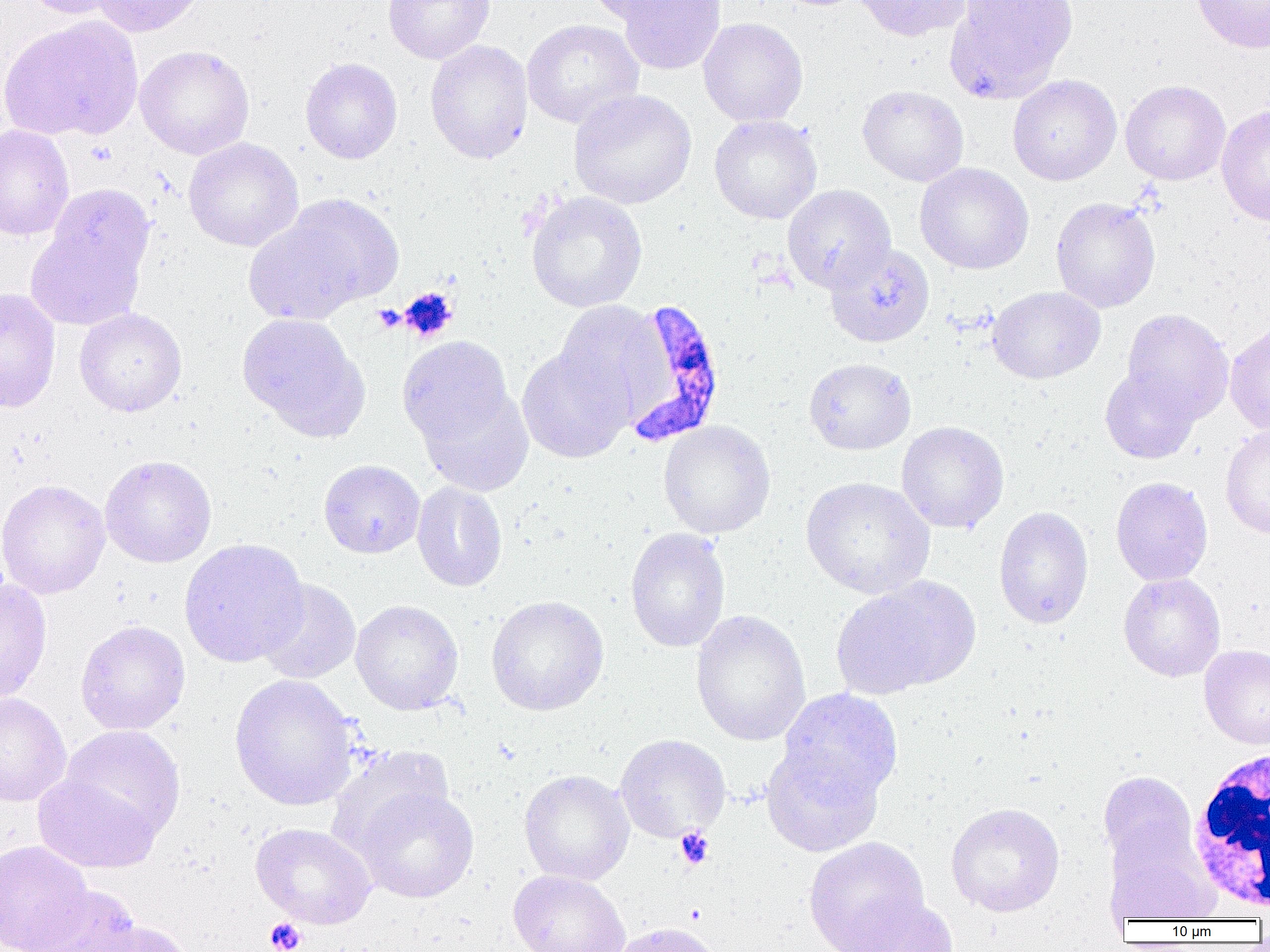
Approximate bounding boxes as (x1,y1)-(x2,y2) corner pairs in pixels. White blood cell locations: (1187,748)-(1270,913). Platelet locations: (397,288)-(458,341), (674,827)-(714,870), (264,917)-(307,952). Plasmodium falciparum-infected red blood cell locations: (619,298)-(727,446). Uninfected red blood cell locations: (21,0)-(131,19), (90,0)-(210,37), (383,0)-(495,64), (585,0)-(697,24), (615,0)-(726,75), (853,0)-(973,42), (945,0)-(1078,100), (1192,0)-(1270,53), (0,17)-(142,141), (698,17)-(808,127), (522,19)-(643,128), (425,39)-(534,164), (134,44)-(255,160), (300,57)-(403,164), (1007,74)-(1122,185), (1120,79)-(1231,186), (857,85)-(969,186), (568,89)-(696,210), (1216,104)-(1270,226), (709,114)-(822,224), (0,125)-(75,241), (183,137)-(304,251), (915,163)-(1034,274), (47,184)-(154,285), (782,184)-(895,293), (525,191)-(647,313), (280,193)-(404,306), (1050,197)-(1161,313), (243,214)-(367,326), (26,223)-(146,331), (824,242)-(935,348), (987,286)-(1105,384), (0,287)-(61,413), (553,300)-(668,424), (74,308)-(187,417), (1122,308)-(1234,423), (237,313)-(367,438), (1225,323)-(1270,435), (397,336)-(514,449), (517,347)-(633,463), (804,358)-(916,455), (1100,365)-(1201,464), (417,385)-(534,496), (658,420)-(776,539), (896,421)-(1009,534), (1220,423)-(1270,539), (99,455)-(217,568), (318,459)-(425,558), (1111,476)-(1213,586), (800,477)-(934,598), (0,479)-(110,600), (411,481)-(507,592), (993,506)-(1094,629), (625,527)-(731,653), (178,538)-(309,668), (1118,573)-(1226,682), (832,577)-(978,697), (0,579)-(52,705), (256,579)-(361,684), (486,595)-(609,716), (350,599)-(464,715), (690,609)-(811,747), (75,620)-(190,735), (1199,645)-(1270,750), (229,674)-(360,811), (777,688)-(904,805), (0,692)-(71,807), (60,725)-(185,840), (615,734)-(731,842), (761,743)-(885,857), (327,745)-(453,858), (518,769)-(634,886), (1097,770)-(1200,878), (33,772)-(160,874), (355,788)-(479,903), (945,802)-(1065,917), (250,823)-(377,929), (804,837)-(929,952), (1105,837)-(1218,924), (0,839)-(93,952), (508,870)-(631,952), (30,886)-(143,952), (840,895)-(958,952), (80,920)-(193,952), (610,921)-(722,952). Slide-level diagnosis: Plasmodium falciparum. Optical microscopy. One field of a larger specimen. Captured at 1000x magnification. Thin blood film. Image is 1270×952 pixels.